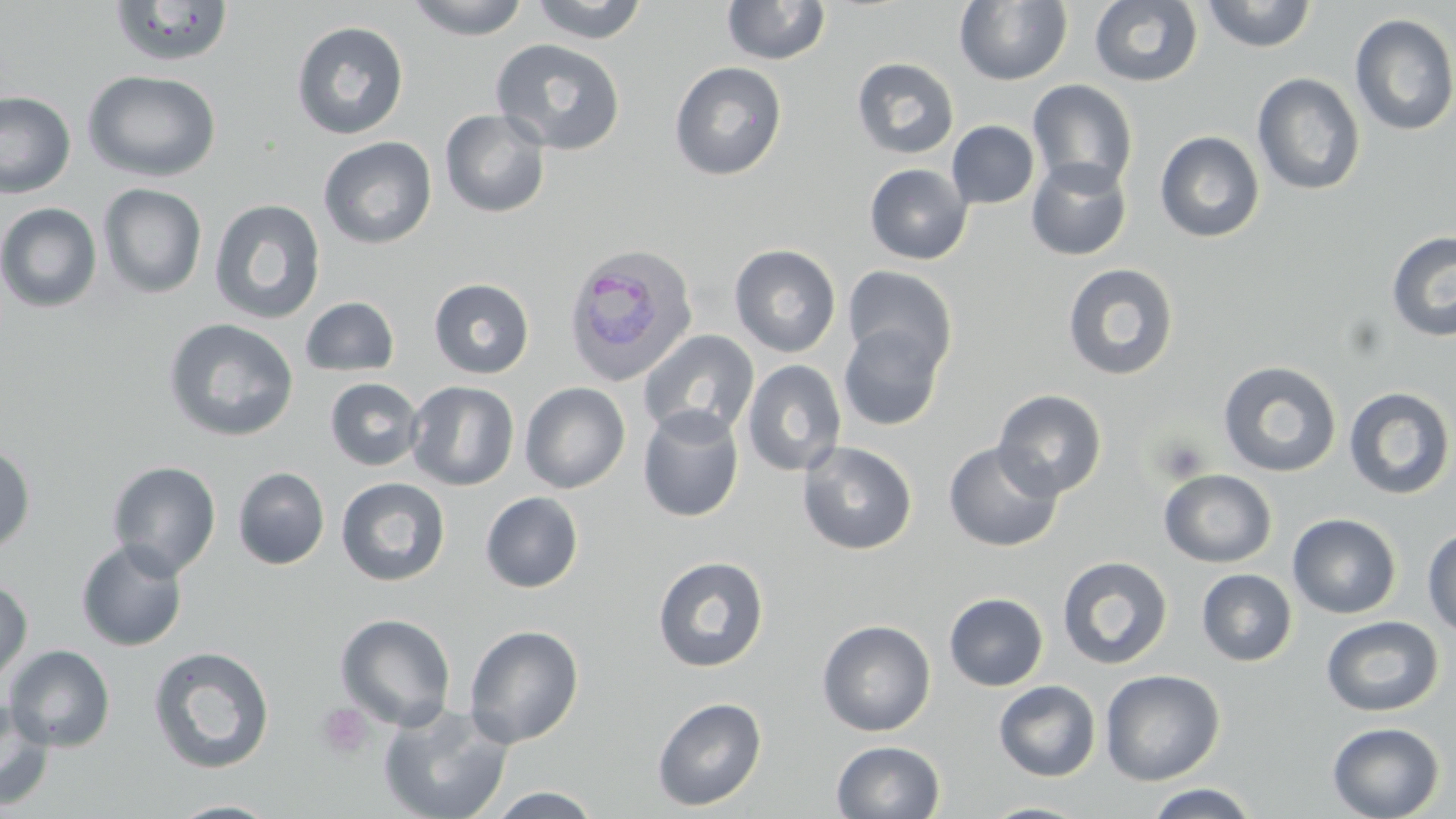
plasmodium_ovale_infected_red_blood_cell_locations: 'approximate bounding boxes as (x1, y1, x2, y2) in pixels: (562, 242, 699, 385)'
slide_level_diagnosis: Plasmodium ovale
uninfected_red_blood_cell_locations: 'approximate bounding boxes as (x1, y1, x2, y2) in pixels: (405, 0, 532, 40), (527, 0, 650, 44), (954, 0, 1073, 86), (1089, 0, 1203, 88), (1200, 0, 1318, 52), (108, 1, 235, 68), (721, 1, 832, 66), (1350, 13, 1456, 137), (291, 21, 409, 140), (490, 38, 627, 156), (852, 57, 960, 160), (669, 61, 788, 181), (82, 70, 221, 182), (1251, 72, 1366, 196), (1027, 79, 1139, 194), (0, 91, 76, 199), (440, 109, 551, 218), (947, 120, 1040, 209), (1155, 131, 1265, 243), (318, 136, 438, 249), (1026, 158, 1132, 260), (864, 163, 972, 265), (97, 183, 208, 299), (209, 198, 326, 324), (0, 202, 103, 313), (1386, 231, 1456, 342), (729, 244, 841, 357), (1062, 262, 1179, 380), (843, 265, 957, 375), (428, 278, 534, 379), (300, 297, 399, 377), (162, 317, 299, 443), (838, 323, 945, 431), (637, 328, 760, 442), (742, 359, 847, 477), (1217, 360, 1343, 478), (325, 377, 424, 471), (406, 381, 520, 491), (520, 382, 630, 494), (1343, 386, 1455, 500), (992, 388, 1108, 500), (637, 406, 745, 522), (943, 440, 1064, 553), (797, 441, 918, 555), (0, 443, 36, 554), (106, 460, 221, 579), (233, 467, 330, 570), (1158, 468, 1278, 568), (335, 477, 450, 587), (480, 491, 584, 593), (1287, 513, 1401, 619), (1422, 527, 1456, 637), (76, 538, 189, 652), (652, 555, 769, 672), (1057, 556, 1173, 670), (1196, 569, 1297, 667), (0, 578, 33, 687), (944, 592, 1048, 691), (335, 612, 456, 731), (1321, 615, 1444, 717), (817, 619, 936, 737), (463, 624, 584, 748), (4, 644, 115, 752), (147, 645, 276, 775), (1100, 669, 1225, 786), (993, 680, 1101, 782), (651, 696, 767, 811), (0, 698, 55, 811), (377, 702, 514, 819), (1327, 722, 1445, 819), (832, 740, 945, 819), (1144, 783, 1260, 818), (484, 787, 603, 818), (164, 799, 285, 818), (978, 801, 1094, 818)'
preparation: thin blood film
platelet_locations: 'approximate bounding boxes as (x1, y1, x2, y2) in pixels: (1150, 434, 1211, 484), (316, 702, 375, 761)'
field_of_view: one of a larger specimen
magnification: 1000x
stain: May-Grünwald-Giemsa
modality: optical microscopy
image_size: 1456×819 pixels